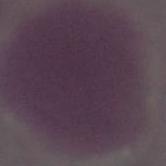
Summary:
  - Modality: photomicrograph
  - Magnification: 1000x
  - Identification: red blood cell